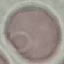

result = no malaria parasites seen
stain = Giemsa
capture = smartphone camera at the microscope eyepiece
preparation = thin blood film
image type = automatically extracted cell patch, resized to 64 × 64 pixels